Comment on the morphology of the erythrocytes.
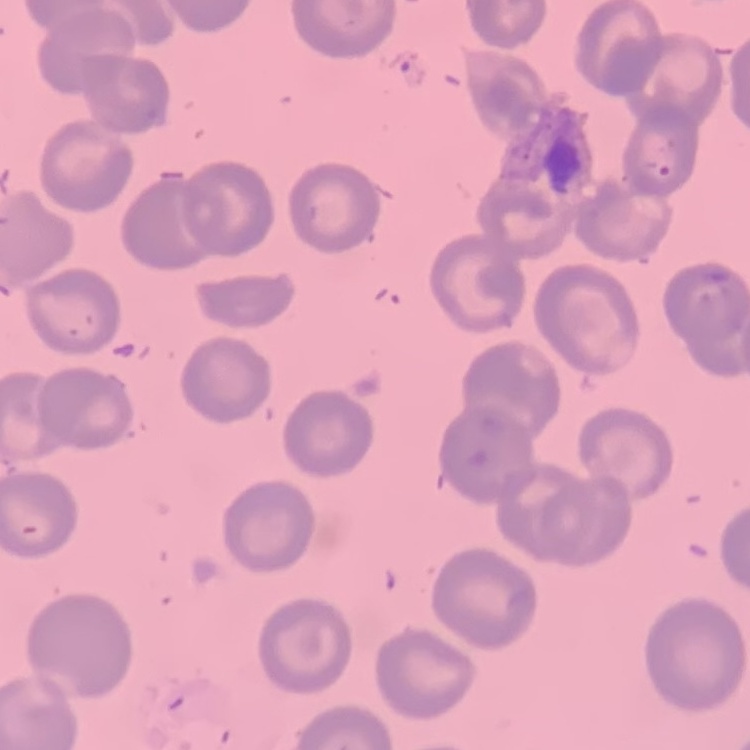

No rouleaux formation.

Thin peripheral smear. Square crop of a larger photomicrograph. Stained with either Field's or Giemsa.